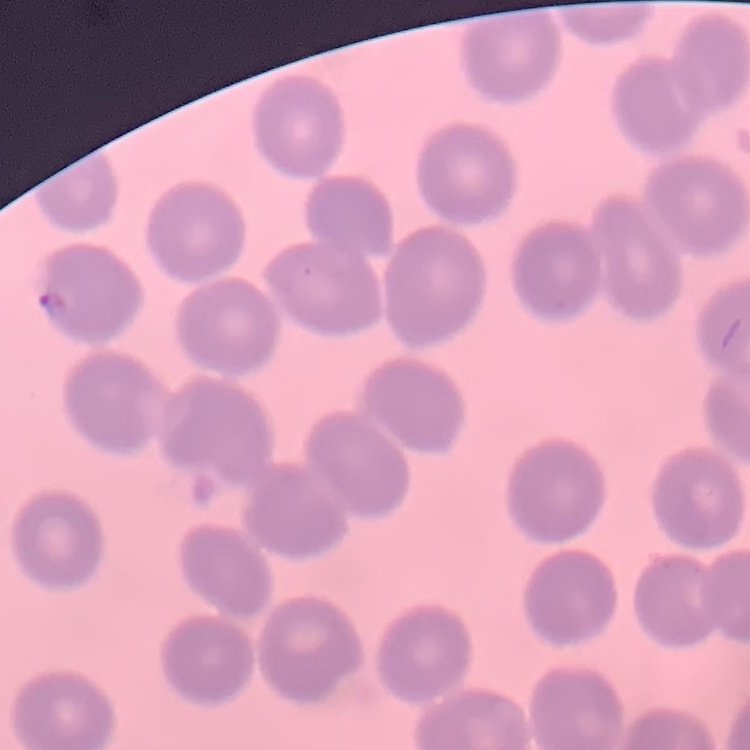 The erythrocytes exhibit no rouleaux formation. Field's or Giemsa stain. Thin blood film. One tile cut from a larger photomicrograph.